Assess this cell for malaria.
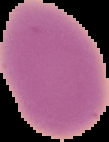
Uninfected.

From a thin blood film. Image is 109×142 pixels. Segmented cell region on a black background.